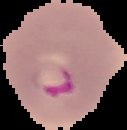
Malaria status: parasitized. Image is 127×130 pixels. From a thin blood film. Cell region segmented out of the field of view; the surrounding area is masked to black.